Identify the parasite.
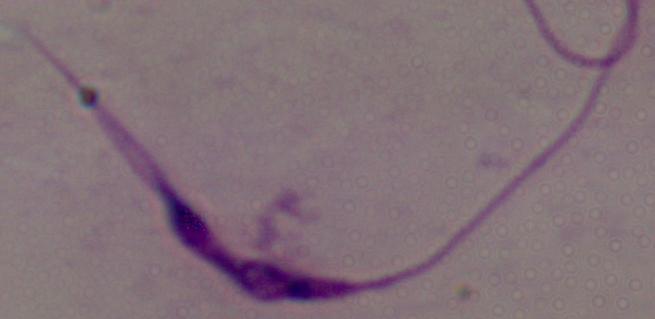
Leishmania.

Micrograph. 1000x magnification.